Give the position of every Plasmodium parasite visible.
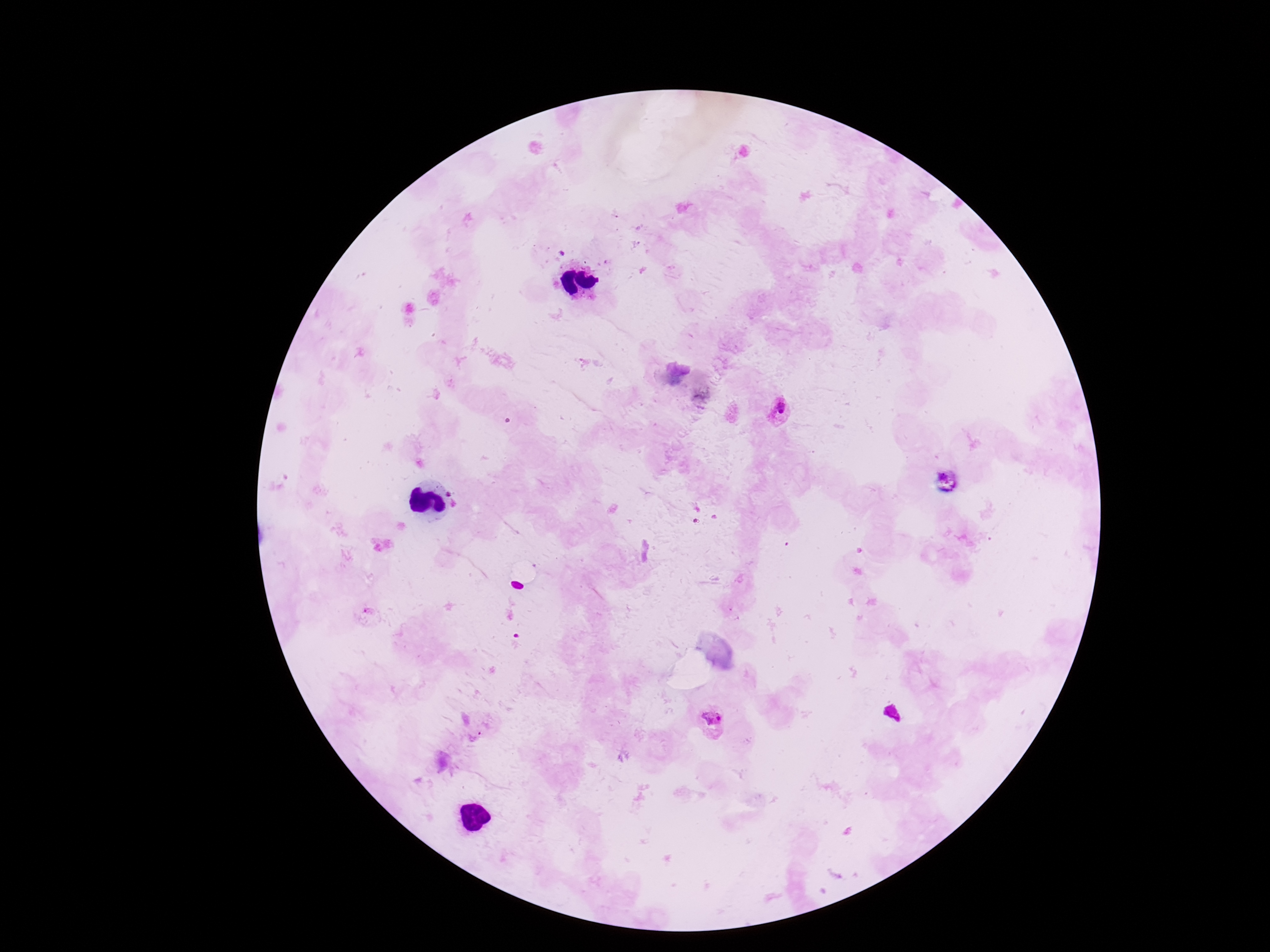

Approximate centers as [x, y] in pixels.
Plasmodium parasites: [780, 412], [712, 724].

Patient malaria status: infected. Photographed through the microscope eyepiece with a smartphone camera. One field from this slide. Giemsa stain. Image is 1270×952 pixels. Thick blood smear. 100x magnification.